Classify this cell by malaria status.
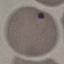
It is uninfected.

Summary:
  - Preparation: thin smear
  - Capture: smartphone through the microscope eyepiece
  - Stain: Giemsa
  - Image type: cell patch, automatically extracted from a larger field of view and resized to 64 × 64 pixels